Evaluate for Plasmodium parasites.
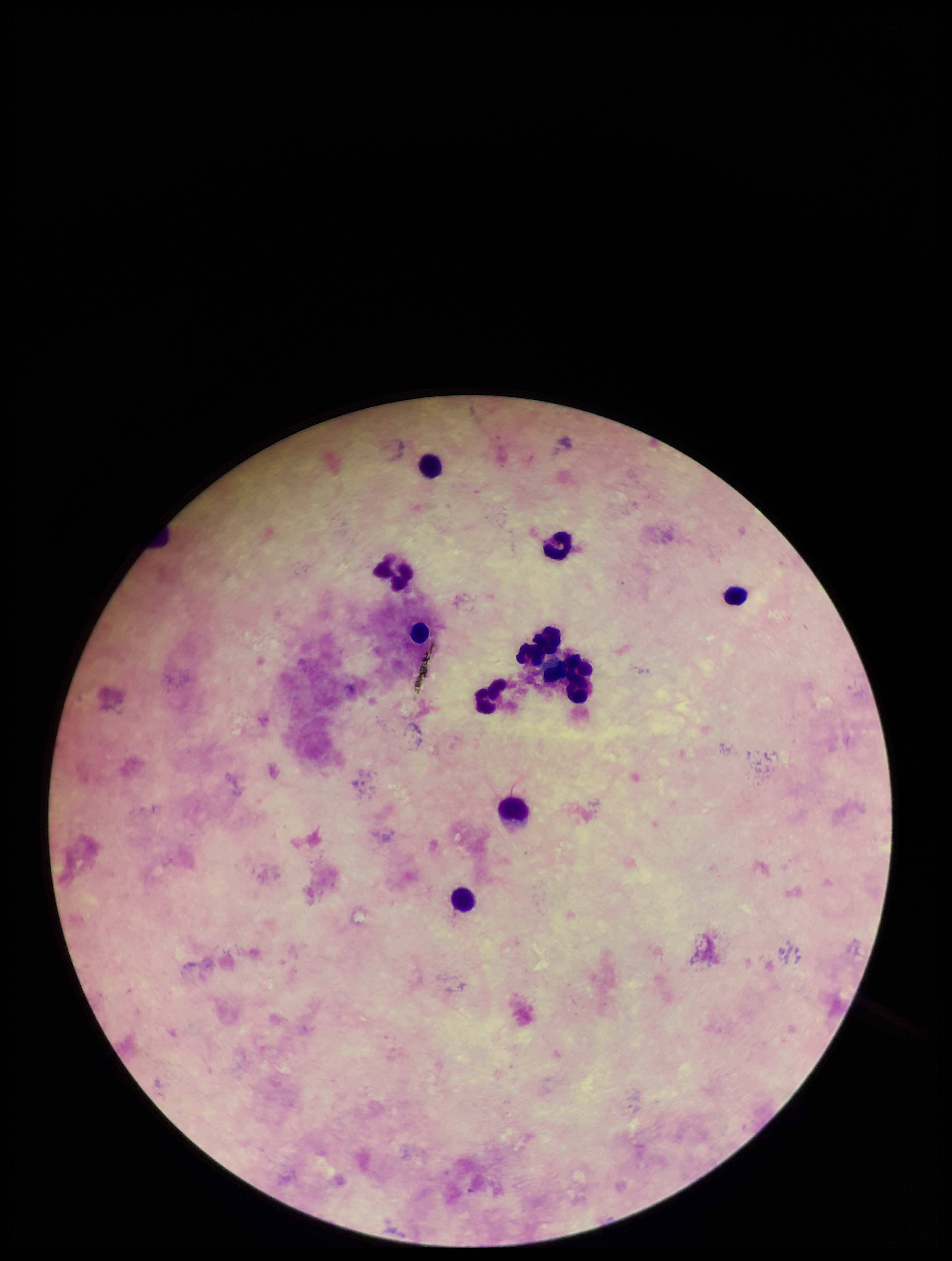

None identified.

leukocyte count = 10
stain = Giemsa
capture = smartphone photograph through the microscope eyepiece
patient malaria status = negative
parasite count = 0
field of view = one from this slide
image size = 952×1261 pixels
preparation = thick smear